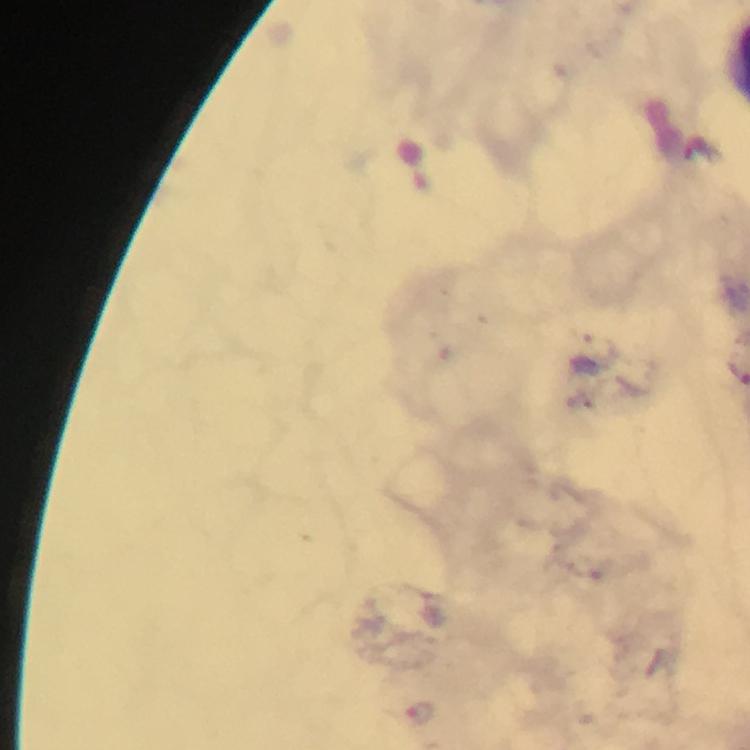 Approximate centers as {x, y} in pixels. Malaria parasite locations: {600, 347}, {421, 712}. Image is 750×750 pixels. From a malaria diagnostic workup. 100x magnification. Thick smear. Photographed with a smartphone mounted on the microscope. Immersion oil was used. Giemsa-stained preparation. A crop from one field of view.